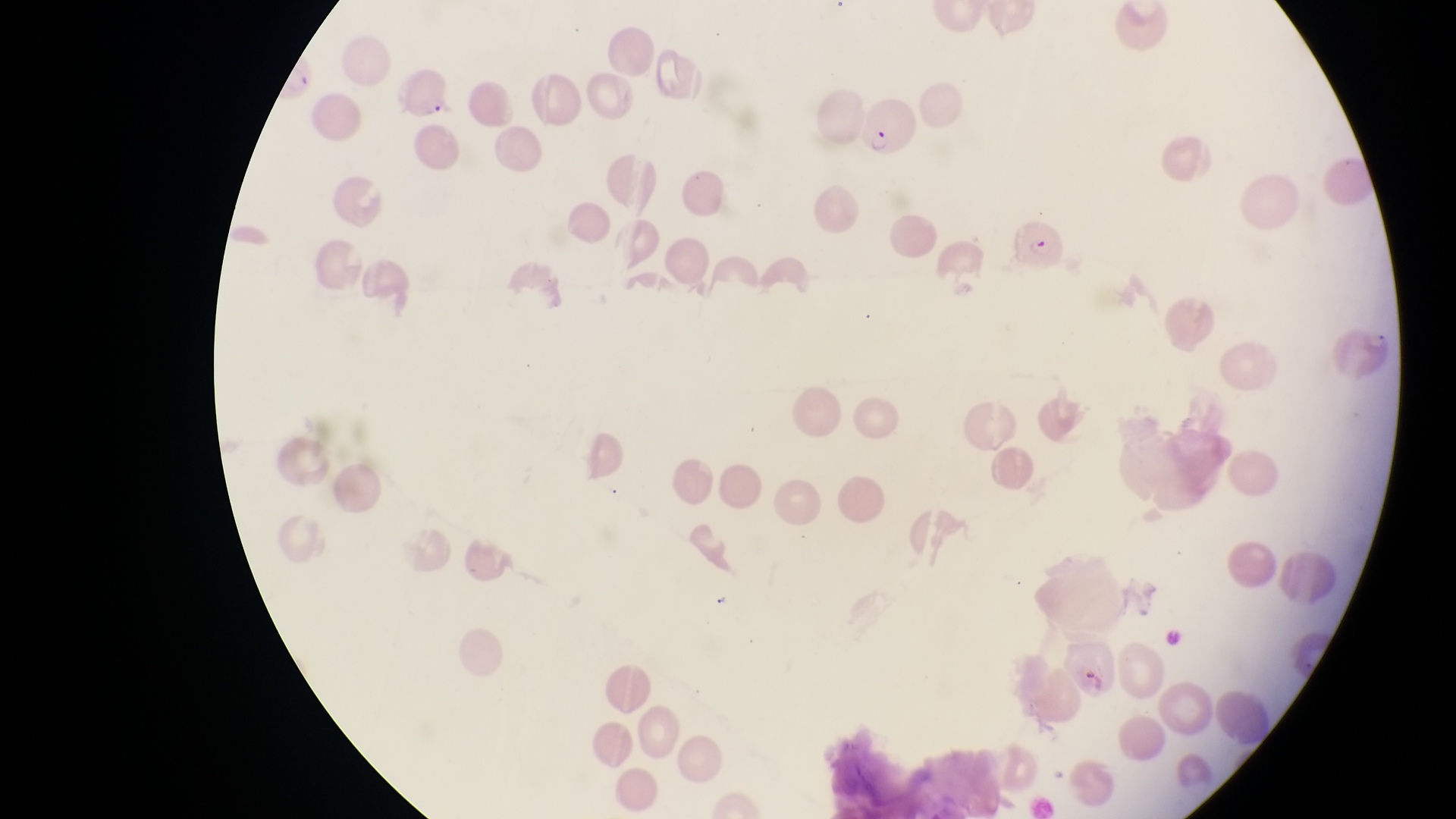
Approximate bounding boxes as left top right bottom in pixels. Parasitised red blood cell locations: 862 102 921 160; 1003 209 1061 273; 1335 315 1395 382; 1053 629 1117 701. Thin blood smear. Photographed through the eyepiece of an Olympus CX-23 microscope with a smartphone camera. At a magnification of 1000x. One field of view. Image is 1456×819 pixels. Collected in Uganda.